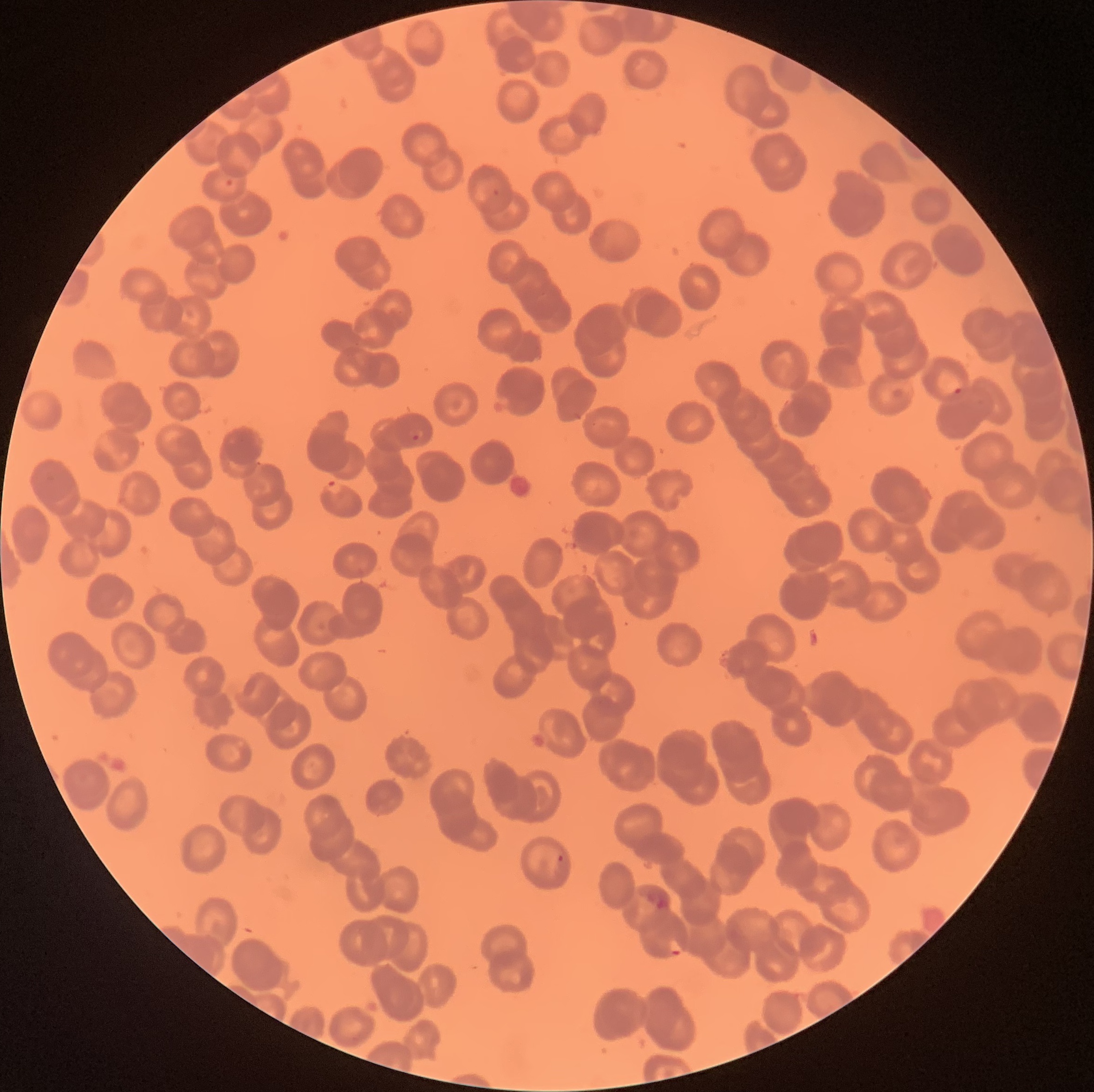

coordinate format = approximate bounding boxes as (x1,y1)-(x2,y2) corner pairs in pixels
Plasmodium parasites too small for a box (approximate centers as (x,y) in pixels) = (496,191), (577,416), (594,424)
Plasmodium parasite locations = (225,179)-(233,186), (953,388)-(963,395), (412,434)-(420,441), (326,480)-(343,495), (557,854)-(564,862), (643,888)-(671,909), (667,939)-(685,956)
preparation = thin blood smear
image size = 1094×1092 pixels
red blood cell morphology = rouleaux formation
modality = optical microscopy